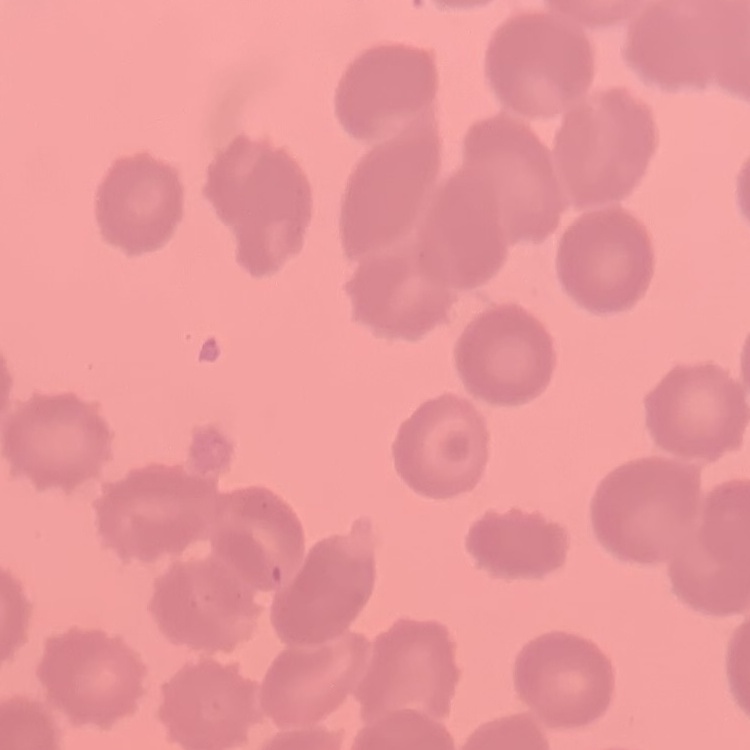

The erythrocytes show no rouleaux formation. Square crop of a larger photomicrograph. Stained with either Field's or Giemsa. Thin peripheral smear.